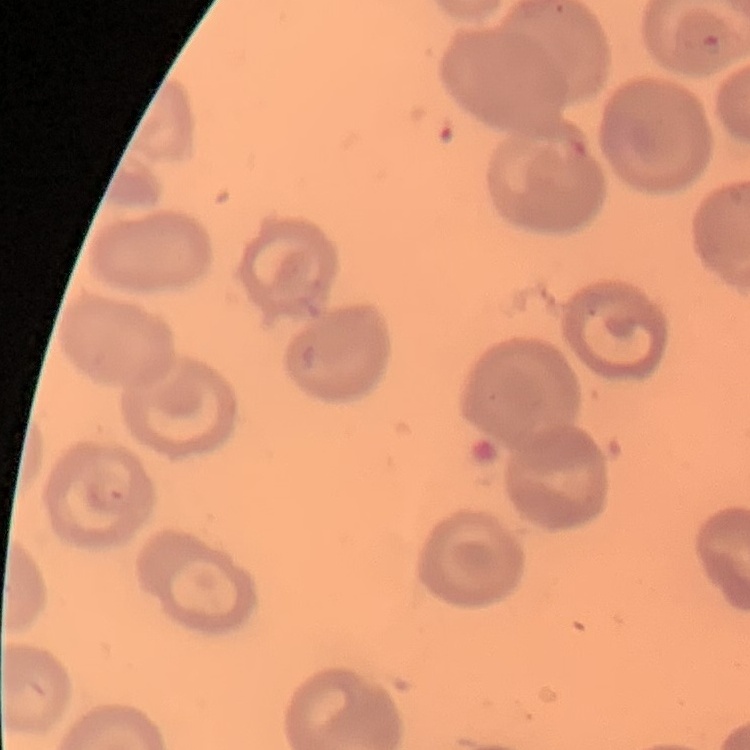
The erythrocytes show no rouleaux formation. Field's or Giemsa stain. One tile cut from a larger photomicrograph. Thin peripheral smear.